Report the malaria status of this cell.
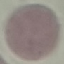

It is uninfected.

Photographed with a smartphone camera at the microscope eyepiece. Thin smear of blood. Automatically extracted cell patch, resized to 64 × 64 pixels. Giemsa stain.